Assess this cell for malaria.
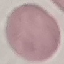

It is uninfected.

Summary:
  - Preparation: thin blood smear
  - Capture: smartphone camera at the microscope eyepiece
  - Image type: cell patch, automatically extracted from a larger field of view and resized to 64 × 64 pixels
  - Stain: Giemsa